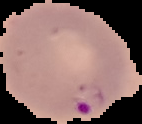
{
  "result": "Plasmodium parasites detected",
  "preparation": "thin blood smear",
  "image_size": "142×124 pixels",
  "image_type": "segmented cell region with the area outside set to black"
}